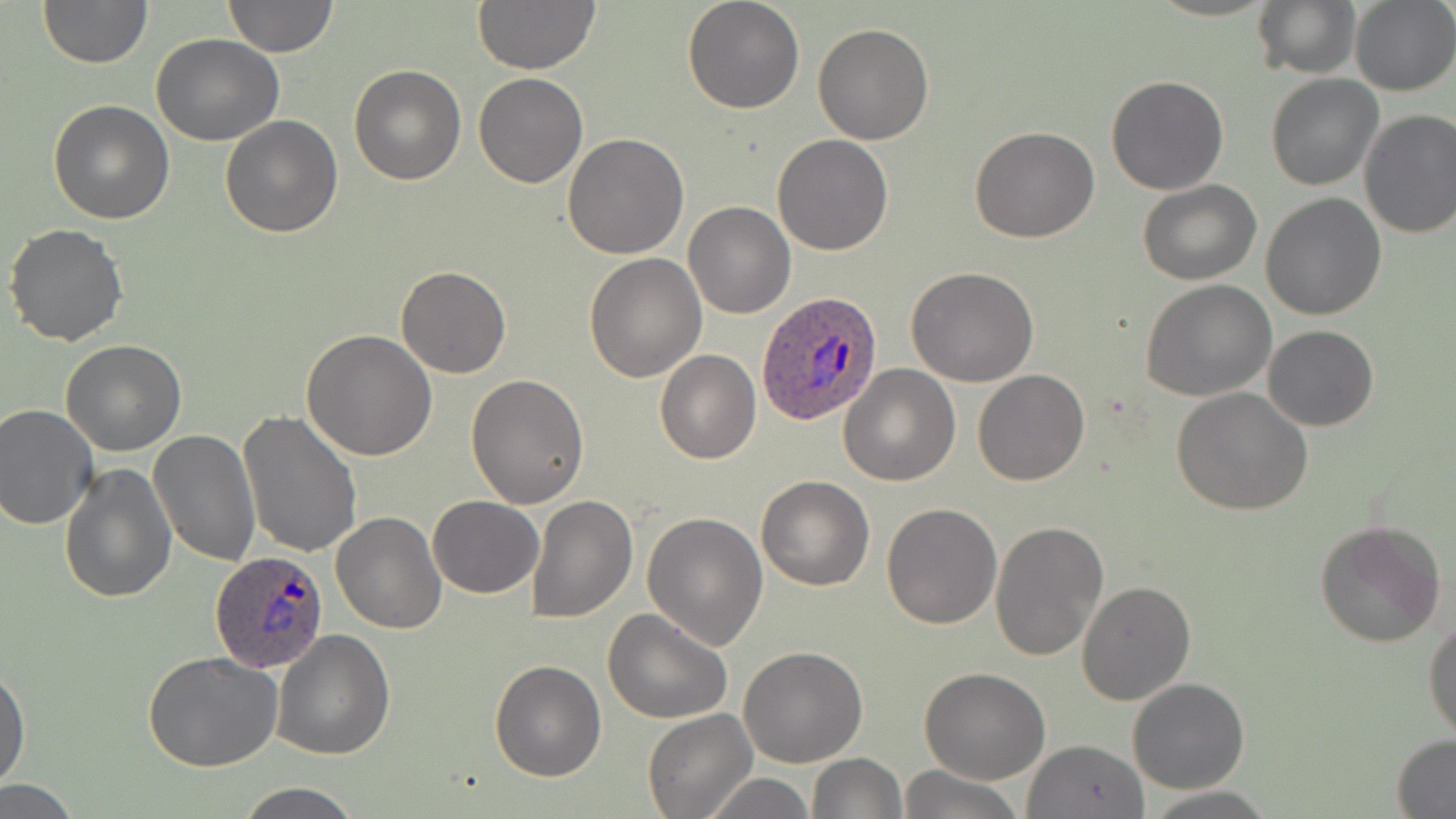 Approximate bounding boxes as (x1,y1)-(x2,y2) corner pairs in pixels. Uninfected red blood cell locations: (37,0)-(152,68), (222,0)-(339,57), (471,0)-(602,75), (682,0)-(804,114), (1251,0)-(1361,79), (1349,2)-(1456,94), (812,22)-(936,146), (151,33)-(284,146), (349,63)-(466,185), (474,73)-(589,188), (1106,74)-(1229,195), (1264,75)-(1382,190), (47,99)-(176,223), (1357,109)-(1456,239), (221,116)-(343,238), (970,127)-(1098,244), (563,134)-(689,259), (771,134)-(894,256), (1137,179)-(1262,285), (1262,191)-(1386,321), (683,201)-(795,318), (4,223)-(129,346), (584,252)-(707,382), (395,266)-(511,379), (906,267)-(1040,387), (1142,280)-(1278,402), (1263,325)-(1379,431), (302,330)-(437,462), (62,339)-(185,455), (655,350)-(761,464), (839,364)-(961,485), (972,368)-(1089,485), (465,373)-(591,508), (1171,386)-(1315,516), (0,402)-(99,530), (238,411)-(363,560), (148,429)-(261,567), (59,462)-(176,603), (755,475)-(874,590), (526,492)-(638,624), (428,495)-(544,598), (881,502)-(1001,629), (332,511)-(448,633), (642,511)-(768,651), (990,518)-(1109,661), (1312,520)-(1445,649), (1076,579)-(1196,704), (603,608)-(733,726), (1424,614)-(1456,744), (273,628)-(395,759), (738,645)-(868,767), (142,652)-(284,772), (489,660)-(606,782), (0,666)-(29,790), (920,667)-(1050,783), (1127,678)-(1250,794), (644,707)-(755,818), (1391,736)-(1456,817), (1022,739)-(1150,818), (807,753)-(907,818), (897,765)-(1022,819), (701,772)-(815,818), (0,781)-(86,816), (234,782)-(366,819), (1144,789)-(1276,817). Plasmodium ovale-infected red blood cell locations: (759,292)-(882,426), (211,550)-(330,672). Slide-level diagnosis: Plasmodium ovale. Captured at 1000x magnification. May-Grünwald-Giemsa-stained preparation. One field of a larger specimen. Thin blood smear. Image is 1456×819 pixels. Optical microscopy.